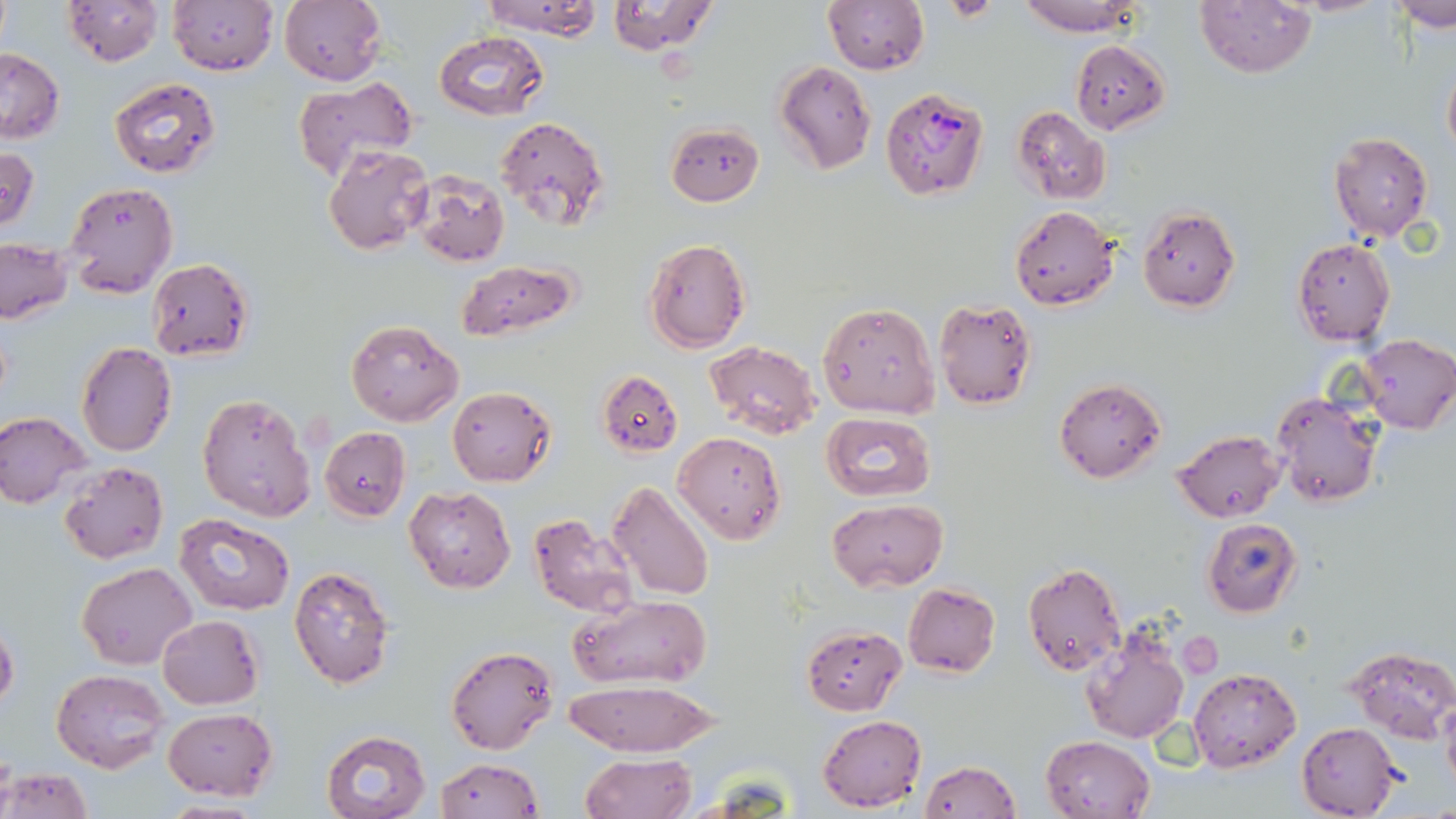

Approximate bounding boxes as named x1/y1/x2/y2 corners in pixels. Uninfected red blood cell locations: (x1=63, y1=0, x2=163, y2=66), (x1=168, y1=0, x2=278, y2=74), (x1=279, y1=0, x2=388, y2=87), (x1=480, y1=0, x2=605, y2=39), (x1=824, y1=0, x2=928, y2=74), (x1=1016, y1=0, x2=1147, y2=36), (x1=1196, y1=0, x2=1315, y2=76), (x1=604, y1=1, x2=721, y2=56), (x1=1387, y1=1, x2=1456, y2=29), (x1=433, y1=30, x2=551, y2=121), (x1=1070, y1=39, x2=1170, y2=133), (x1=0, y1=49, x2=64, y2=145), (x1=1442, y1=57, x2=1456, y2=162), (x1=774, y1=60, x2=877, y2=175), (x1=108, y1=76, x2=221, y2=179), (x1=292, y1=77, x2=419, y2=178), (x1=1012, y1=106, x2=1110, y2=204), (x1=494, y1=116, x2=610, y2=234), (x1=664, y1=121, x2=765, y2=206), (x1=1328, y1=131, x2=1434, y2=241), (x1=1, y1=145, x2=39, y2=233), (x1=322, y1=145, x2=432, y2=256), (x1=411, y1=171, x2=511, y2=268), (x1=64, y1=180, x2=177, y2=298), (x1=1010, y1=205, x2=1120, y2=310), (x1=1137, y1=208, x2=1240, y2=312), (x1=643, y1=237, x2=752, y2=354), (x1=0, y1=238, x2=72, y2=324), (x1=1292, y1=238, x2=1395, y2=347), (x1=148, y1=258, x2=254, y2=362), (x1=458, y1=260, x2=579, y2=340), (x1=933, y1=299, x2=1037, y2=410), (x1=817, y1=302, x2=939, y2=419), (x1=346, y1=318, x2=464, y2=427), (x1=1357, y1=334, x2=1456, y2=435), (x1=703, y1=341, x2=822, y2=440), (x1=76, y1=342, x2=177, y2=456), (x1=597, y1=369, x2=683, y2=456), (x1=1055, y1=378, x2=1166, y2=482), (x1=447, y1=386, x2=557, y2=485), (x1=198, y1=391, x2=316, y2=522), (x1=1272, y1=392, x2=1383, y2=507), (x1=0, y1=411, x2=92, y2=508), (x1=822, y1=411, x2=936, y2=504), (x1=320, y1=426, x2=410, y2=521), (x1=1174, y1=429, x2=1286, y2=522), (x1=673, y1=430, x2=786, y2=545), (x1=59, y1=462, x2=168, y2=566), (x1=607, y1=482, x2=715, y2=603), (x1=404, y1=485, x2=516, y2=594), (x1=828, y1=498, x2=947, y2=592), (x1=527, y1=510, x2=641, y2=620), (x1=174, y1=513, x2=294, y2=616), (x1=1202, y1=517, x2=1303, y2=617), (x1=78, y1=562, x2=197, y2=669), (x1=1022, y1=563, x2=1128, y2=677), (x1=288, y1=565, x2=396, y2=688), (x1=903, y1=582, x2=1000, y2=677), (x1=570, y1=593, x2=713, y2=689), (x1=157, y1=615, x2=264, y2=709), (x1=0, y1=620, x2=18, y2=713), (x1=802, y1=623, x2=906, y2=715), (x1=1078, y1=626, x2=1192, y2=745), (x1=445, y1=644, x2=558, y2=755), (x1=1344, y1=645, x2=1455, y2=744), (x1=1189, y1=667, x2=1301, y2=771), (x1=51, y1=668, x2=170, y2=773), (x1=563, y1=679, x2=720, y2=758), (x1=1441, y1=699, x2=1456, y2=797), (x1=162, y1=707, x2=279, y2=802), (x1=816, y1=715, x2=926, y2=811), (x1=1297, y1=722, x2=1402, y2=818), (x1=321, y1=729, x2=431, y2=819), (x1=1040, y1=734, x2=1156, y2=819), (x1=578, y1=752, x2=696, y2=819), (x1=434, y1=757, x2=542, y2=819), (x1=918, y1=761, x2=1019, y2=818), (x1=1, y1=767, x2=93, y2=819), (x1=156, y1=801, x2=269, y2=819). Plasmodium falciparum-infected red blood cell locations: (x1=880, y1=87, x2=989, y2=200). Slide-level diagnosis: Plasmodium falciparum. Image is 1456×819 pixels. 1000x magnification. Thin blood film. One field of a larger specimen. Optical microscopy. May-Grünwald-Giemsa stain.